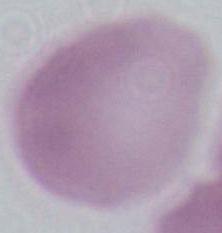
identification = erythrocyte
magnification = 1000x
modality = micrograph